Evaluate for Plasmodium parasites.
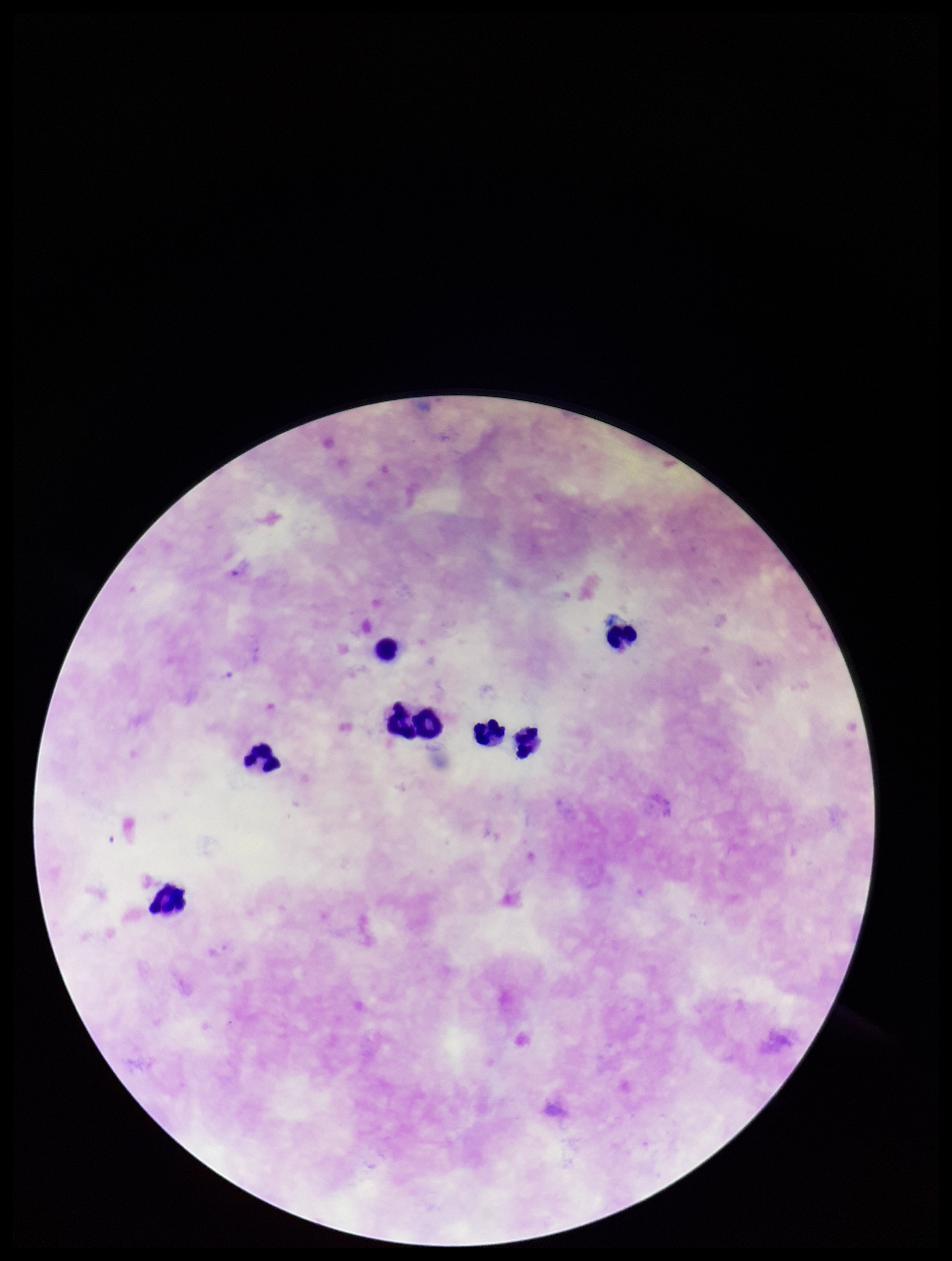
None identified.

Summary:
  - Field of view: one from this slide
  - Patient malaria status: infected
  - Preparation: thick smear
  - Image size: 952×1261 pixels
  - Parasite count: 0
  - Stain: Giemsa
  - Species reported for this patient: Plasmodium falciparum
  - Capture: smartphone photograph through the microscope eyepiece
  - Leukocyte count: 8